Identify the parasite.
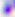

This is Toxoplasma gondii.

Captured at 400x magnification. Micrograph.